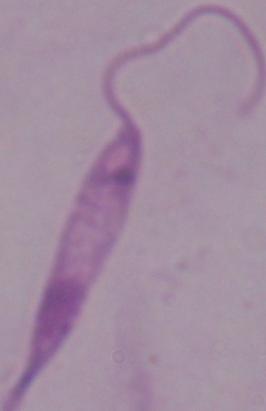

magnification: 1000x
identification: Leishmania
modality: photomicrograph